Locate every malaria parasite by life-cycle stage, and every leukocyte.
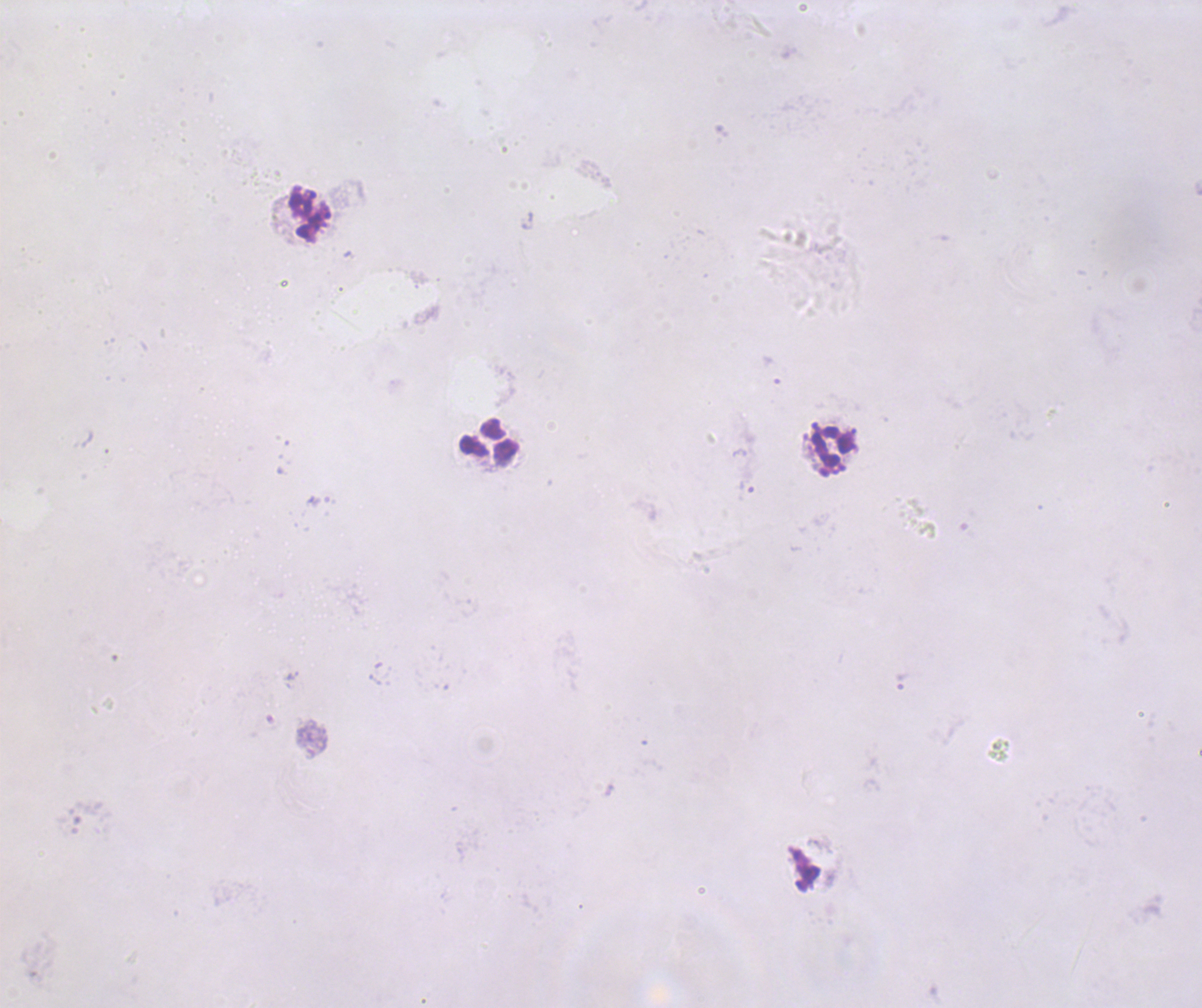
Approximate centers as {x, y} in pixels.
Trophozoites: {747, 486}, {900, 682}.
No schizont or gametocyte forms observed.
Leukocytes: {309, 213}, {490, 441}, {833, 451}.

Summary:
  - Context: previously used in an actual diagnosis
  - Stain: Romanowsky
  - Preparation: thick blood smear
  - Field of view: single
  - Magnification: 100x
  - Image size: 1202×1008 pixels
  - Coloration quality: bad
  - Background quality: poor